State which parasite is depicted.
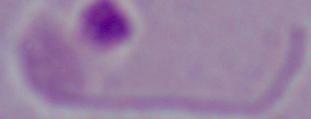
This is Leishmania.

magnification = 1000x
modality = micrograph